Classify this cell by malaria status.
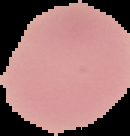
Uninfected.

preparation = thin blood film
image type = cell region segmented out of the field of view; surrounding area masked to black
image size = 130×136 pixels